Report the malaria status of this cell.
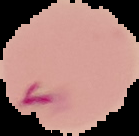
It is parasitized.

Summary:
  - Preparation: thin blood smear
  - Image type: segmented cell region on a black background
  - Image size: 139×136 pixels